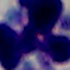 A leukocyte is shown. Photomicrograph. 1000x magnification.